Identify the cell.
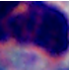
A leukocyte.

modality = micrograph
magnification = 1000x